Classify this cell by malaria status.
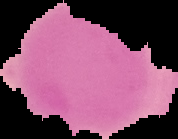

It is uninfected.

image size = 178×139 pixels
preparation = thin blood smear
image type = segmented cell region on a black background